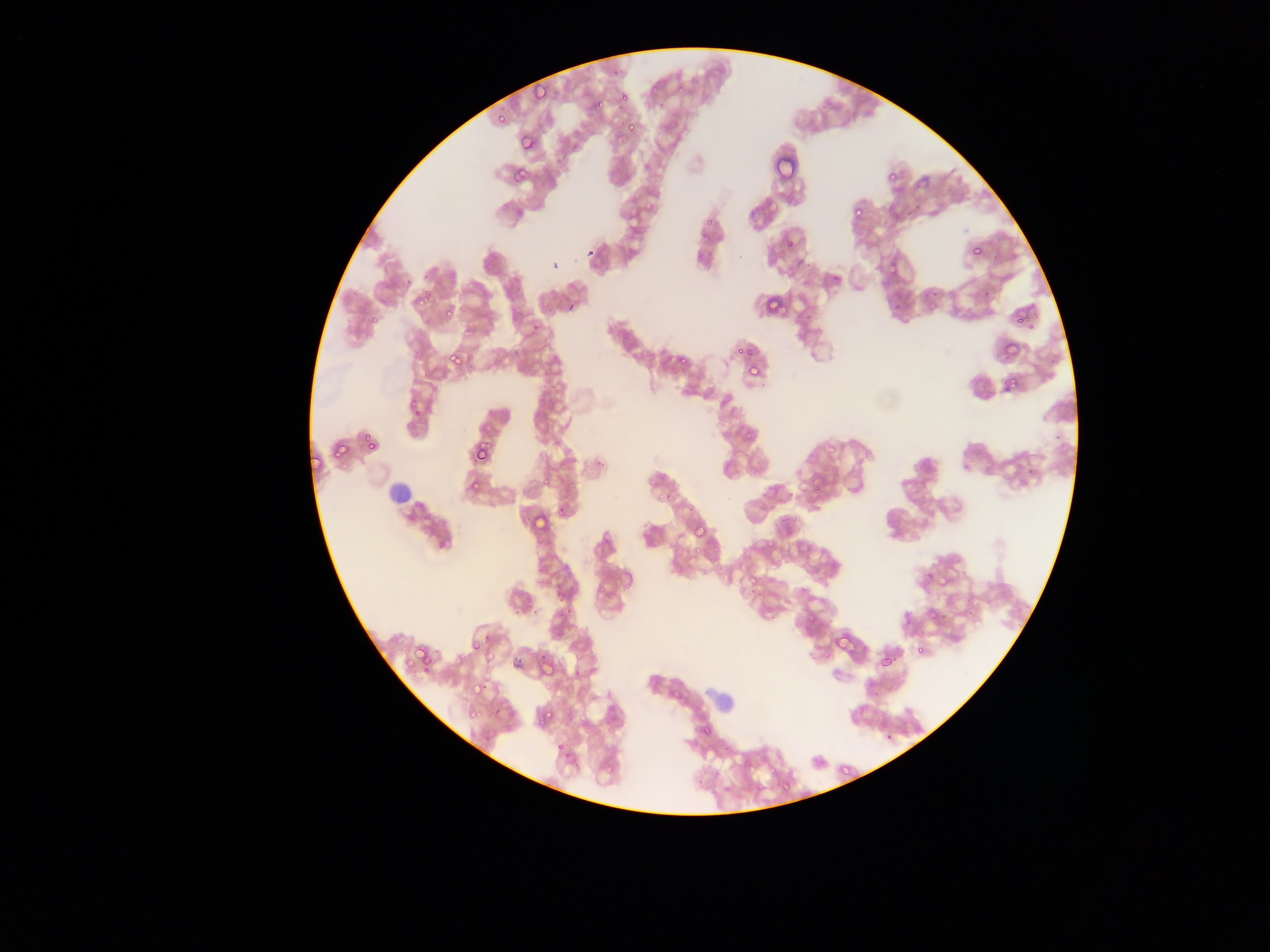
{
  "field_of_view": "single",
  "capture": "mobile-phone photograph through a microscope",
  "image_size": "1270×952 pixels",
  "malaria_parasite_locations": "approximate bounding boxes as [left, top, right, bottom] in pixels: [588, 65, 595, 73], [611, 70, 619, 75], [532, 82, 552, 100], [619, 95, 628, 101], [596, 99, 604, 108], [495, 113, 503, 122], [627, 119, 635, 131], [519, 133, 530, 152], [514, 166, 529, 181], [888, 175, 896, 180], [752, 207, 763, 213], [853, 207, 863, 215], [699, 230, 710, 239], [786, 239, 794, 246], [972, 248, 981, 254], [887, 261, 898, 273], [425, 290, 433, 296], [762, 290, 777, 311], [417, 298, 425, 307], [445, 308, 453, 316], [370, 315, 376, 324], [1016, 319, 1024, 325], [462, 327, 470, 336], [415, 347, 423, 358], [735, 348, 744, 356], [745, 348, 756, 355], [448, 350, 468, 371], [677, 357, 688, 368], [749, 368, 757, 374], [1002, 380, 1018, 392], [409, 396, 416, 407], [414, 407, 423, 416], [364, 435, 370, 443], [340, 441, 351, 455], [367, 443, 375, 451], [473, 443, 491, 463], [311, 450, 327, 472], [596, 458, 604, 466], [653, 471, 663, 477], [471, 480, 481, 490], [814, 484, 825, 493], [665, 493, 676, 499], [534, 507, 554, 530], [559, 507, 569, 516], [780, 512, 791, 522], [788, 512, 799, 521], [692, 523, 707, 534], [693, 546, 700, 554], [926, 571, 933, 579], [547, 576, 553, 585], [749, 576, 755, 586], [557, 593, 567, 602], [565, 605, 573, 616], [836, 634, 857, 650], [472, 639, 482, 648], [484, 644, 500, 662], [413, 646, 424, 663], [918, 646, 922, 654], [540, 652, 546, 660], [879, 655, 892, 668], [403, 659, 414, 669], [574, 670, 578, 678], [485, 677, 491, 685], [544, 683, 551, 691], [471, 685, 479, 694], [671, 690, 678, 698], [546, 709, 556, 718], [467, 710, 478, 717], [704, 726, 711, 736], [563, 737, 572, 751], [719, 738, 728, 754], [573, 764, 581, 773], [603, 764, 618, 774], [839, 766, 851, 777], [784, 781, 793, 792], [724, 782, 730, 791], [757, 784, 763, 792] | approximate [x, y] pixel centers of objects too small to bound: [679, 88], [707, 222], [461, 308], [931, 309], [1029, 329], [335, 454], [964, 467], [547, 481], [653, 481], [661, 496], [715, 548], [519, 610], [943, 617], [435, 653], [425, 674], [541, 719], [557, 747]",
  "preparation": "thin blood film",
  "country": "Ghana"
}